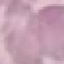
result = no malaria parasites detected
stain = Giemsa
preparation = thin blood film
image type = automatically extracted cell patch, resized to 64 × 64 pixels
capture = smartphone camera at the microscope eyepiece